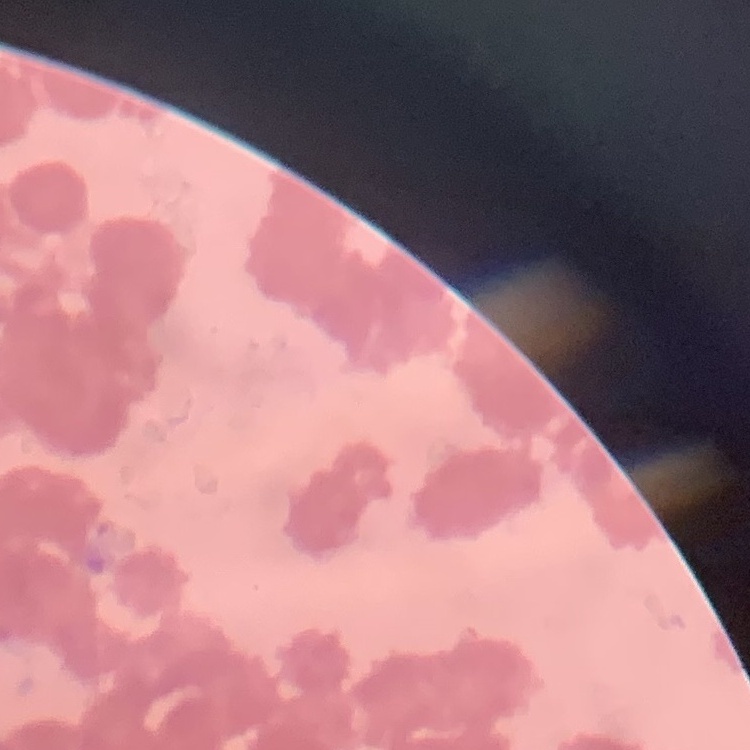

Summary:
  - Erythrocyte morphology: rouleaux formation
  - Stain: Field's or Giemsa
  - Preparation: thin peripheral smear
  - Image type: square crop of a larger photomicrograph